Report the malaria status of this cell.
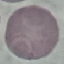
Uninfected.

Acquired by smartphone through the microscope eyepiece. Giemsa-stained preparation. Thin smear of blood. Automatically extracted cell patch, resized to 64 × 64 pixels.